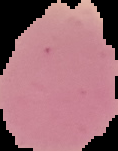
Image is 118×151 pixels. From a thin blood film. The area outside the segmented cell region is set to black. Malaria status: uninfected.